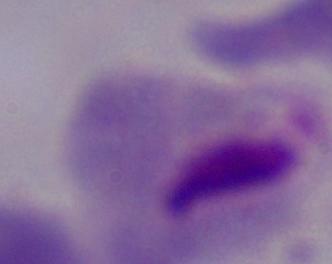
{
  "magnification": "1000x",
  "modality": "photomicrograph",
  "identification": "trichomonad"
}